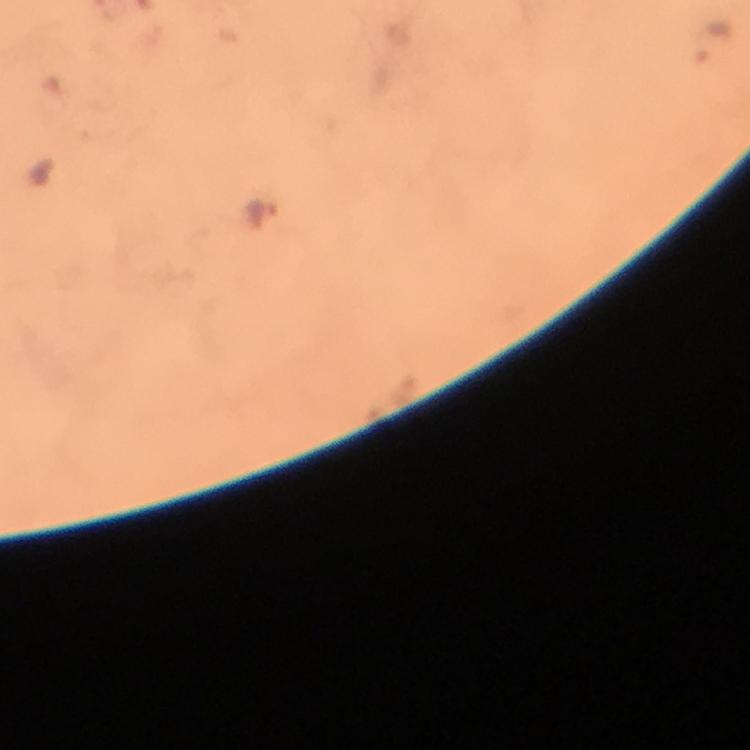

Approximate centers as {x, y} in pixels.
Summary:
  - Plasmodium parasite locations: {709, 42}, {264, 219}
  - Image size: 750×750 pixels
  - Capture: smartphone photograph through a microscope
  - Immersion oil: used
  - Magnification: 100x
  - Stain: Giemsa
  - Cropped from: a single field of view
  - Preparation: thick blood film
  - Context: from a diagnostic examination for malaria